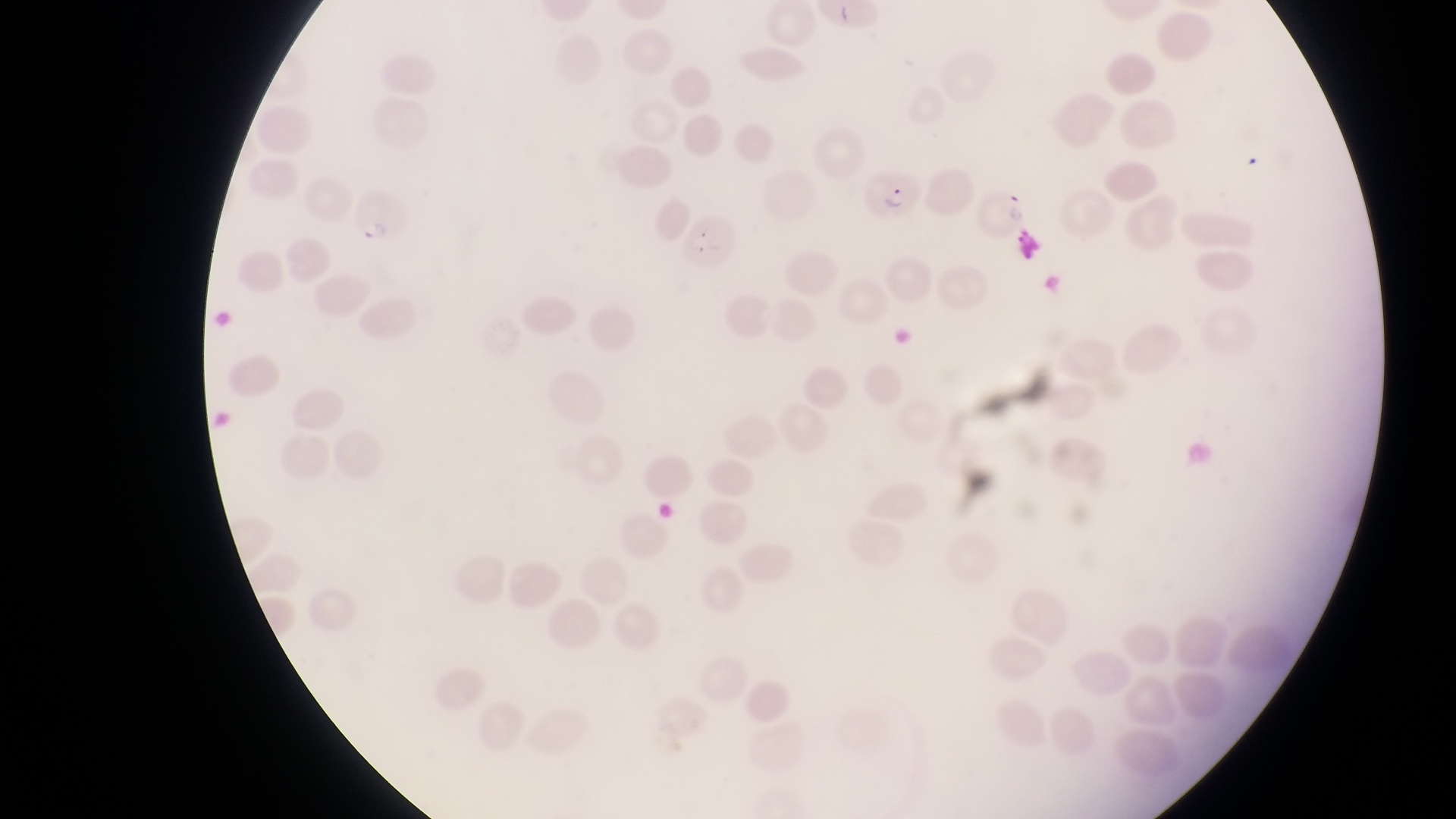
Approximate bounding boxes as {left, top, right, bottom} in pixels. Parasitised red blood cell locations: {864, 159, 925, 222}, {981, 185, 1030, 243}, {347, 190, 410, 250}, {682, 211, 741, 278}. Photographed through the eyepiece of an Olympus CX-23 microscope with a smartphone camera. One field of view. Collected in Uganda. Thin blood film. Image is 1456×819 pixels. At a magnification of 1000x.